Give the position of every malaria parasite.
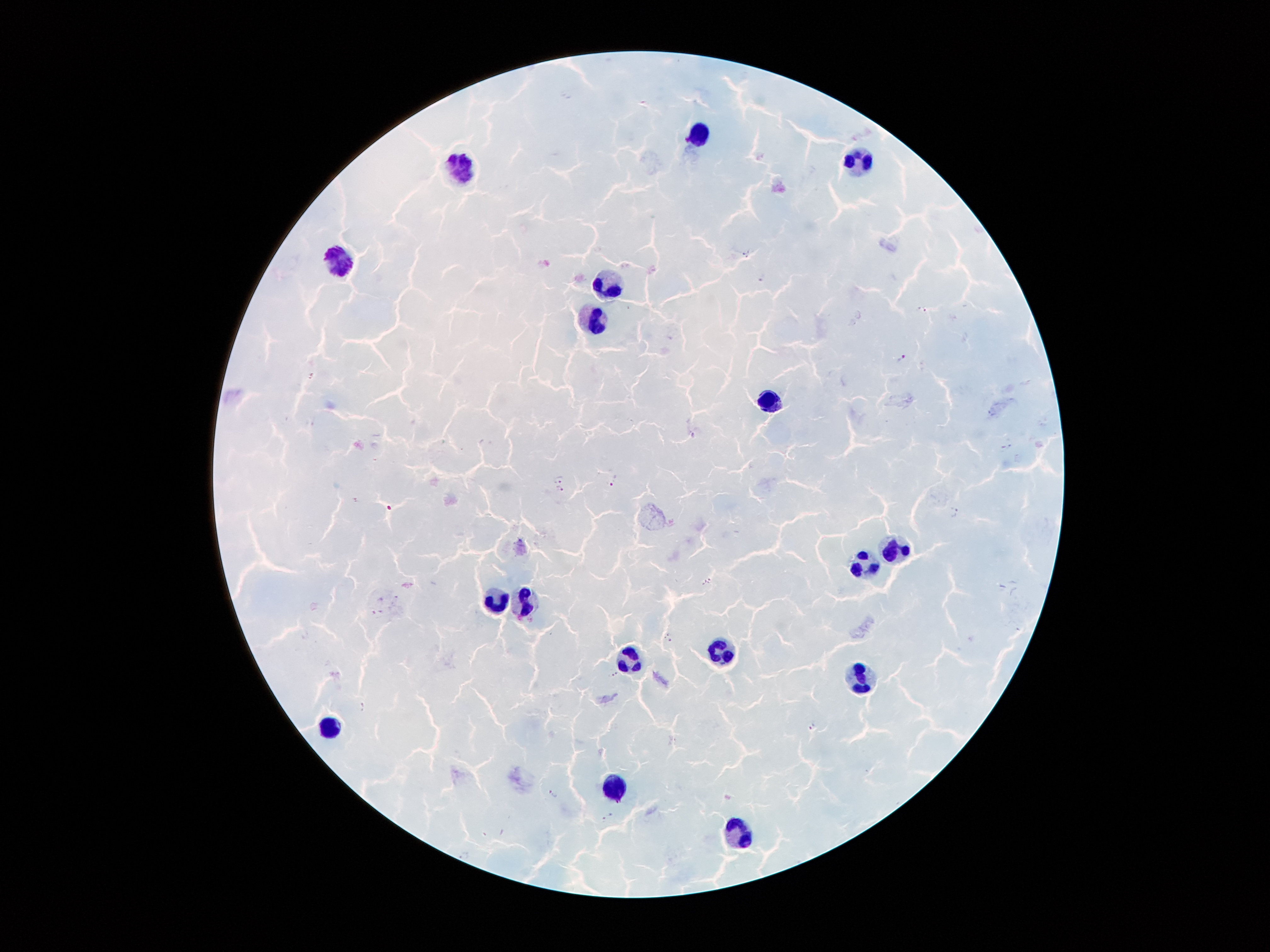
Approximate centers as (x, y) in pixels.
Malaria parasites: (747, 254), (762, 277), (922, 309), (902, 360), (312, 376), (1009, 441), (1000, 450), (559, 479), (614, 479), (561, 491), (956, 512), (708, 581), (395, 597), (381, 598), (382, 612), (372, 613), (669, 637), (615, 674), (362, 705), (812, 727), (553, 793), (607, 817).

Leukocyte locations: (703, 136), (864, 158), (462, 168), (336, 263), (610, 282), (592, 318), (769, 401), (895, 554), (865, 563), (497, 600), (525, 601), (717, 650), (632, 654), (861, 677), (330, 726), (617, 789), (736, 833). 100x magnification. Thick peripheral-blood smear. Smartphone photograph taken through the microscope eyepiece. Giemsa-stained preparation. Single field of view. Image is 1270×952 pixels. Patient malaria status: positive for Plasmodium falciparum.